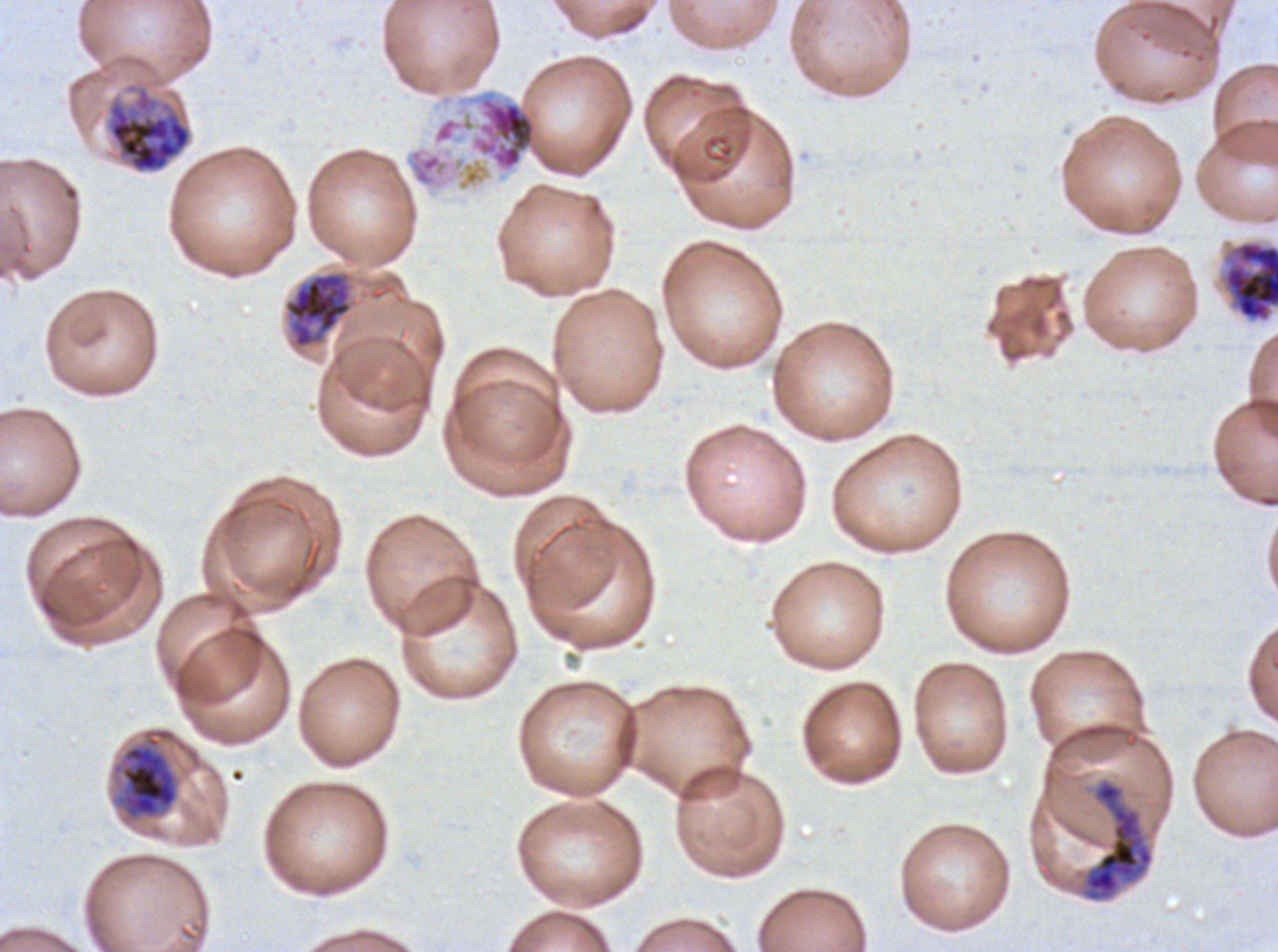

Approximate bounding boxes as {x1, y1, x2, y2} in pixels.
Summary:
  - Segmenter locations: {473, 95, 537, 171}
  - Early schizont locations: {104, 81, 193, 175}, {284, 272, 352, 348}, {120, 745, 178, 818}
  - Late schizont locations: {1222, 239, 1277, 323}, {1084, 779, 1154, 899}
  - Preparation: thin blood film
  - Field of view: sub-image separated from a larger composite
  - Stain: Giemsa
  - Specimen: Plasmodium falciparum from a patient in The Gambia, cultured ex vivo for 24 to 48 hours
  - Image size: 1278×952 pixels
  - Life-cycle stages observed: early schizont, late schizont, segmenter